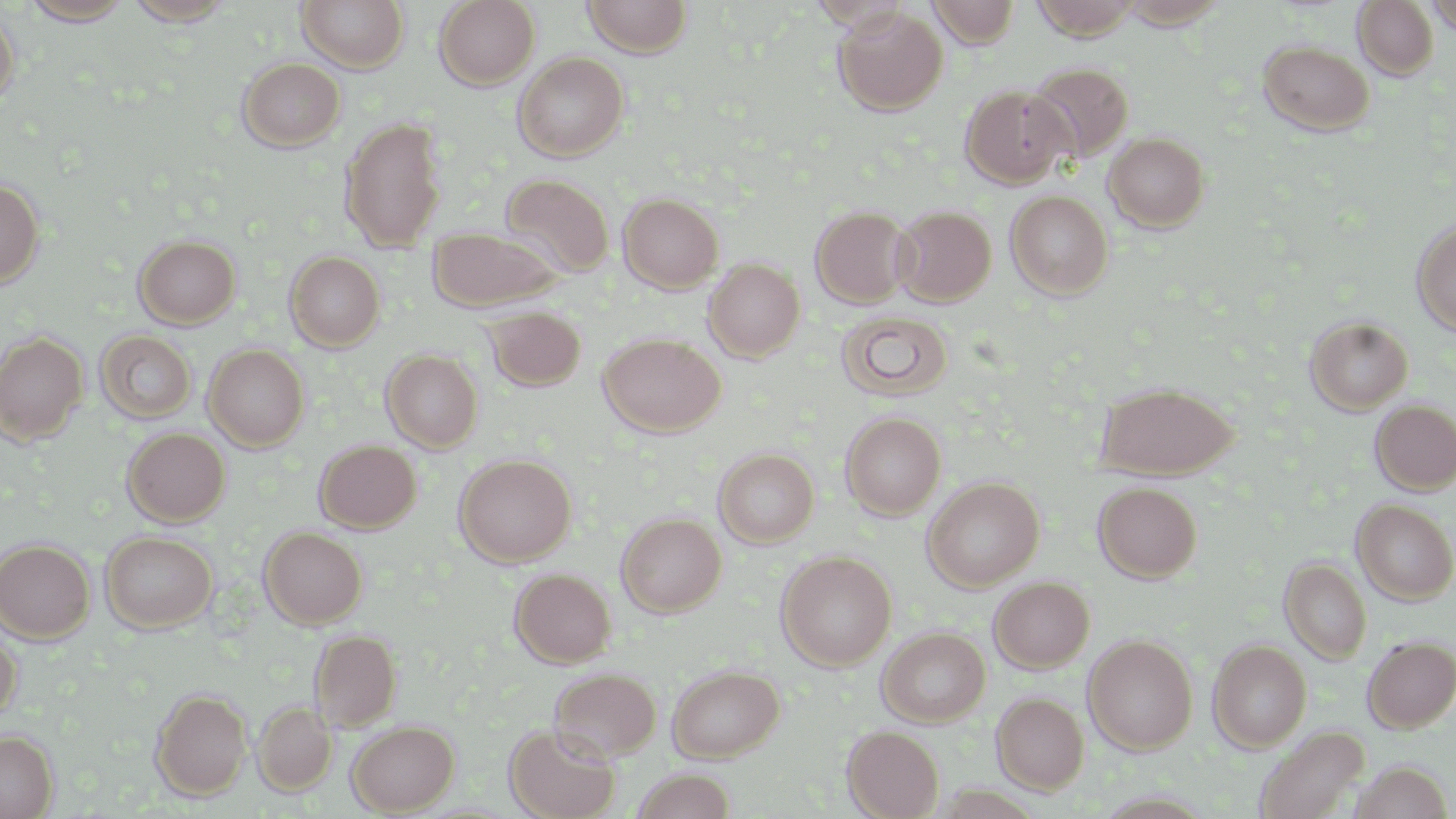

slide_level_diagnosis: no evidence of blood parasites
field_of_view: single
preparation: thin blood film
stain: May-Grünwald-Giemsa
modality: optical microscopy
uninfected_red_blood_cell_locations: 'approximate bounding boxes as [x1, y1, x2, y2] in pixels: [21, 0, 134, 24], [122, 0, 239, 26], [296, 0, 408, 72], [434, 0, 540, 89], [582, 0, 693, 57], [927, 0, 1020, 48], [1032, 0, 1143, 40], [1353, 0, 1438, 80], [1426, 0, 1456, 36], [832, 6, 948, 115], [0, 8, 19, 110], [1258, 40, 1374, 136], [513, 52, 628, 162], [237, 57, 346, 151], [1026, 62, 1133, 164], [960, 85, 1071, 187], [340, 117, 446, 251], [1104, 131, 1211, 232], [500, 174, 615, 279], [0, 178, 44, 289], [1005, 190, 1113, 299], [619, 193, 723, 292], [892, 204, 996, 305], [810, 205, 912, 308], [1412, 219, 1456, 336], [428, 228, 561, 311], [134, 235, 241, 329], [285, 251, 385, 351], [703, 258, 804, 361], [483, 307, 586, 391], [838, 311, 954, 401], [1305, 316, 1413, 414], [94, 330, 197, 424], [0, 331, 88, 444], [598, 333, 726, 437], [203, 344, 309, 451], [381, 349, 483, 452], [1096, 381, 1240, 478], [1370, 399, 1456, 495], [841, 412, 946, 520], [122, 427, 230, 526], [314, 439, 422, 532], [714, 448, 819, 547], [454, 454, 576, 566], [923, 476, 1045, 591], [1093, 481, 1202, 583], [1352, 499, 1456, 604], [617, 513, 726, 616], [259, 527, 367, 628], [100, 531, 218, 633], [0, 538, 95, 643], [777, 550, 897, 670], [1279, 558, 1372, 664], [510, 568, 616, 667], [989, 576, 1094, 673], [877, 626, 990, 726], [0, 628, 21, 722], [309, 629, 402, 731], [1083, 635, 1198, 755], [1362, 636, 1456, 732], [1208, 639, 1312, 751], [667, 664, 784, 763], [549, 668, 662, 762], [150, 687, 252, 799], [991, 692, 1089, 793], [254, 701, 336, 794], [346, 720, 459, 814], [504, 723, 620, 819], [843, 726, 944, 818], [1255, 726, 1369, 819], [0, 731, 57, 818], [1350, 761, 1454, 819], [631, 769, 737, 818]'
magnification: 1000x
image_size: 1456×819 pixels